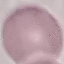
{
  "malaria_status": "uninfected",
  "stain": "Giemsa",
  "preparation": "thin blood smear",
  "image_type": "cell patch, automatically extracted from a larger field of view and resized to 64 × 64 pixels",
  "capture": "smartphone through the microscope eyepiece"
}